Locate every blood parasite and identify its species.
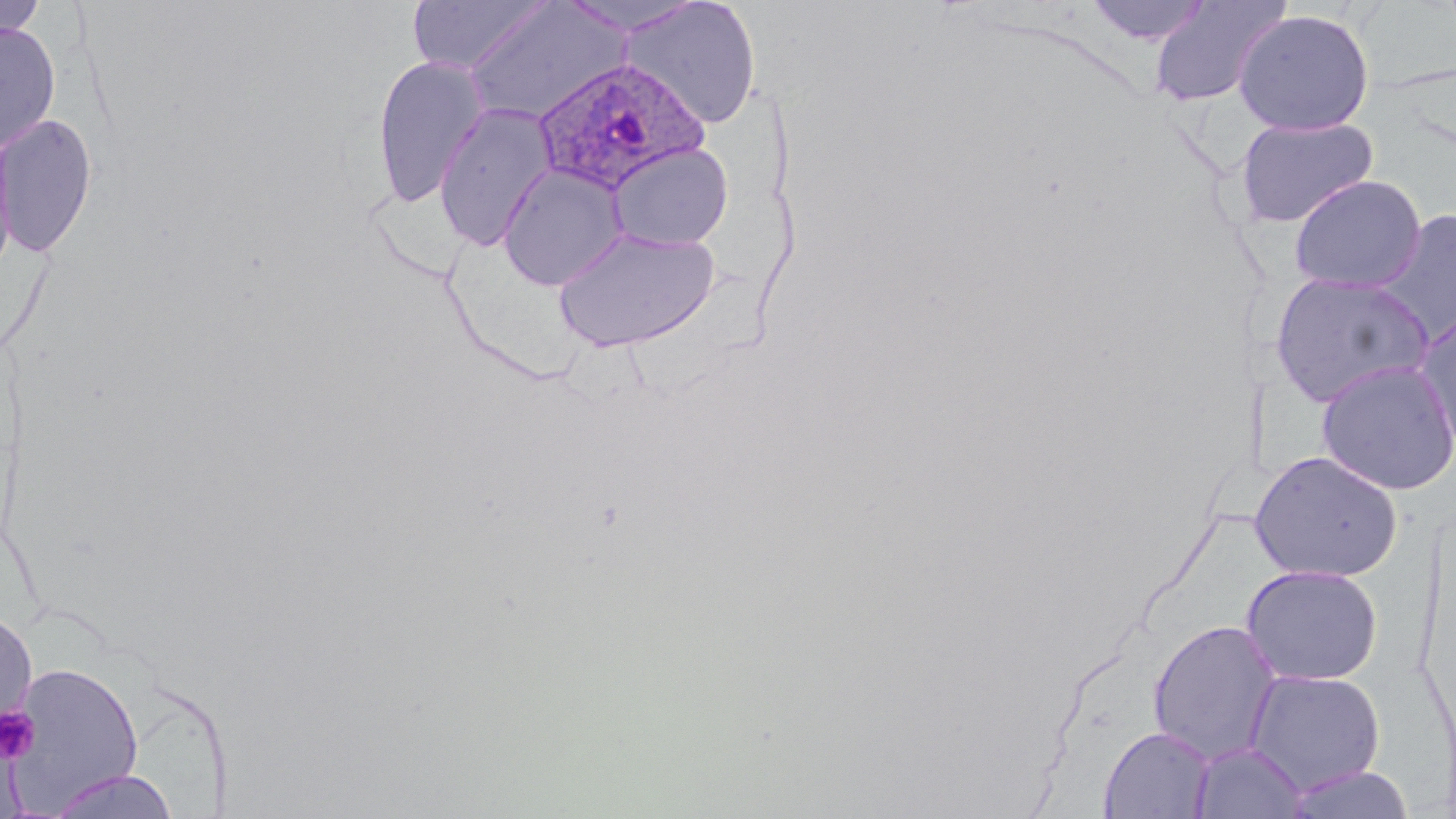

Approximate bounding boxes as (x1, y1, x2, y2) in pixels.
Plasmodium ovale-infected red blood cells: (531, 57, 709, 195).
No Plasmodium falciparum, Plasmodium malariae, Plasmodium vivax, Babesia divergens, or Trypanosoma brucei observed.

Platelet locations: (0, 706, 40, 764). Uninfected red blood cell locations: (0, 0, 47, 42), (557, 0, 707, 36), (621, 0, 762, 129), (1083, 0, 1216, 46), (1147, 0, 1293, 107), (406, 1, 551, 75), (464, 1, 629, 124), (1233, 9, 1375, 136), (0, 21, 61, 154), (371, 54, 489, 208), (435, 102, 557, 250), (0, 113, 98, 259), (1233, 115, 1379, 229), (0, 129, 18, 280), (606, 142, 733, 250), (498, 163, 629, 291), (1288, 174, 1426, 293), (1370, 208, 1456, 347), (552, 225, 721, 352), (1269, 271, 1435, 408), (1413, 311, 1456, 459), (1316, 358, 1456, 495), (1250, 450, 1403, 583), (1241, 564, 1383, 686), (0, 607, 39, 739), (1147, 619, 1282, 764), (6, 661, 144, 810), (1245, 669, 1386, 795), (1099, 726, 1215, 818), (1191, 741, 1307, 818), (1283, 765, 1415, 819), (43, 769, 183, 819). Slide-level diagnosis: Plasmodium ovale. Light microscopy. One field of a larger specimen. Image is 1456×819 pixels. May-Grünwald-Giemsa stain. Thin blood film. 1000x magnification.